Describe the morphology of the red blood cells.
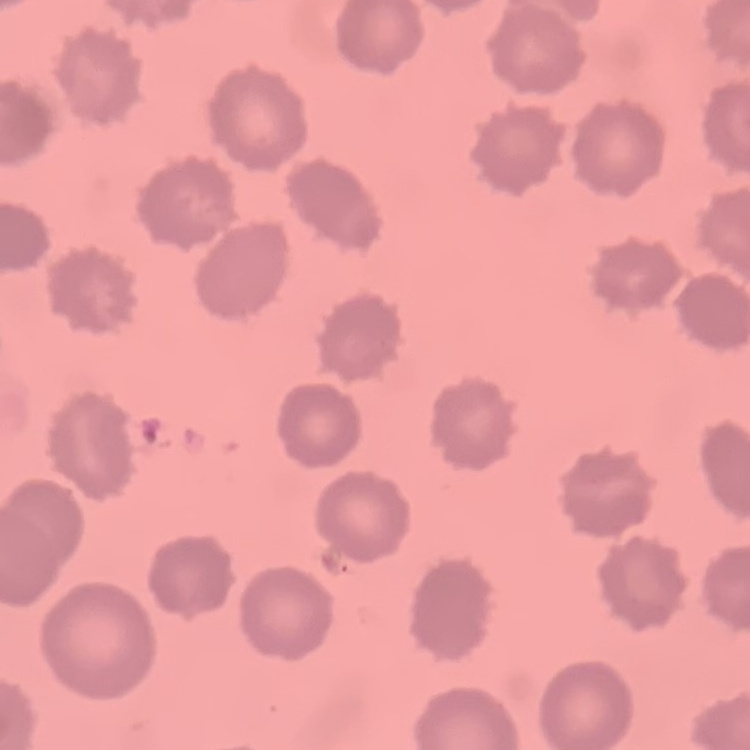
They show no rouleaux formation.

Summary:
  - Image type: square crop of a larger photomicrograph
  - Stain: Field's or Giemsa
  - Preparation: thin blood smear